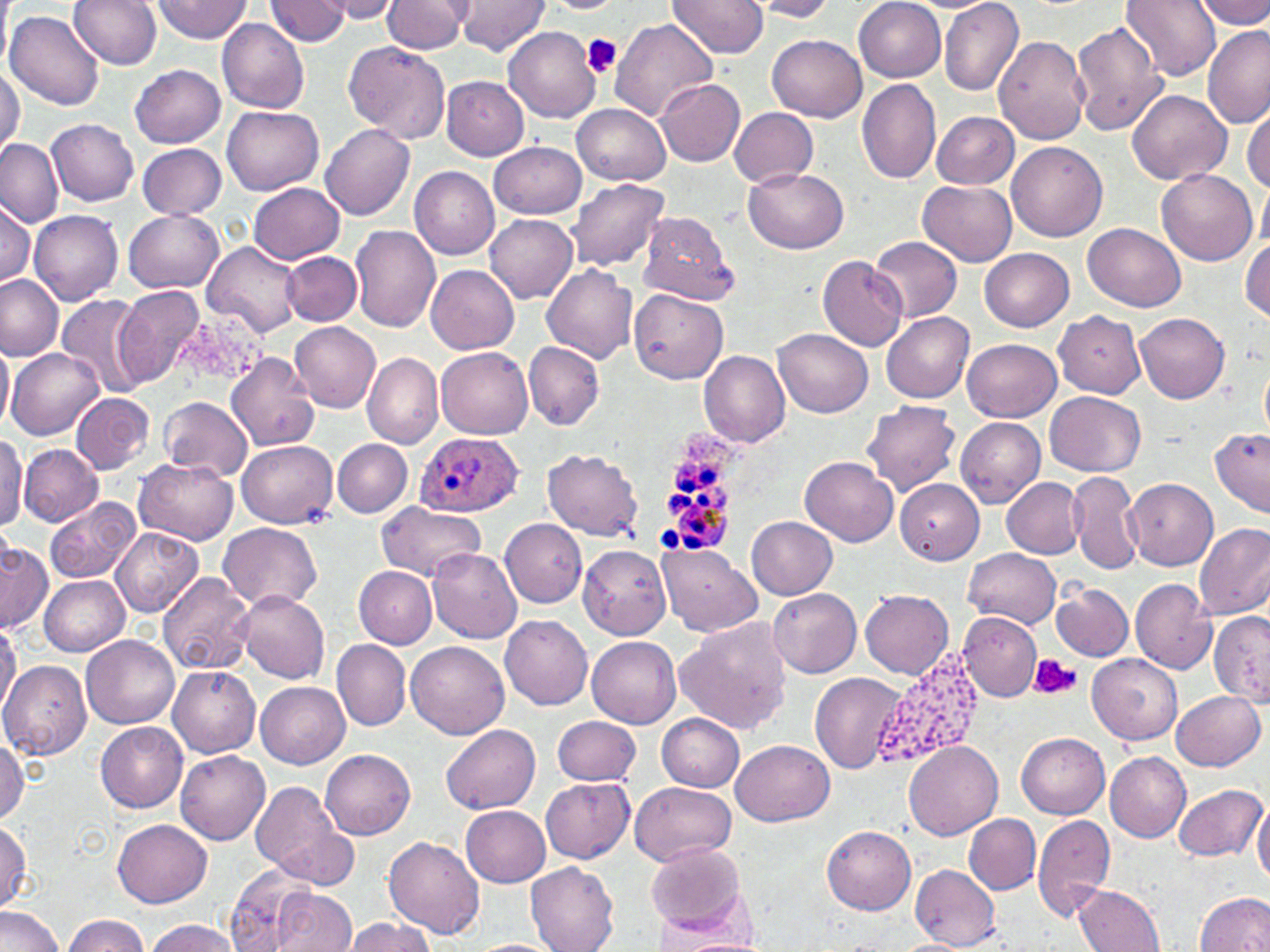

Approximate bounding boxes as named x1/y1/x2/y2 corners in pixels. Platelet locations: (x1=582, y1=34, x2=623, y2=79), (x1=1030, y1=655, x2=1083, y2=700). Uninfected red blood cell locations: (x1=0, y1=0, x2=10, y2=75), (x1=71, y1=0, x2=163, y2=69), (x1=319, y1=0, x2=404, y2=21), (x1=383, y1=0, x2=471, y2=53), (x1=455, y1=0, x2=550, y2=57), (x1=669, y1=0, x2=769, y2=57), (x1=1124, y1=0, x2=1221, y2=81), (x1=1196, y1=0, x2=1270, y2=30), (x1=151, y1=1, x2=252, y2=44), (x1=264, y1=1, x2=352, y2=44), (x1=539, y1=1, x2=625, y2=14), (x1=748, y1=1, x2=838, y2=21), (x1=854, y1=1, x2=945, y2=81), (x1=940, y1=1, x2=1024, y2=96), (x1=5, y1=9, x2=104, y2=109), (x1=607, y1=17, x2=718, y2=123), (x1=216, y1=18, x2=309, y2=115), (x1=1071, y1=19, x2=1169, y2=136), (x1=1201, y1=25, x2=1269, y2=126), (x1=503, y1=26, x2=600, y2=122), (x1=767, y1=32, x2=868, y2=120), (x1=993, y1=35, x2=1091, y2=145), (x1=342, y1=41, x2=450, y2=144), (x1=131, y1=64, x2=226, y2=147), (x1=0, y1=65, x2=25, y2=158), (x1=441, y1=76, x2=529, y2=160), (x1=655, y1=79, x2=745, y2=166), (x1=857, y1=79, x2=942, y2=185), (x1=1126, y1=89, x2=1230, y2=187), (x1=572, y1=104, x2=670, y2=185), (x1=1244, y1=104, x2=1270, y2=193), (x1=224, y1=106, x2=324, y2=197), (x1=730, y1=106, x2=818, y2=188), (x1=932, y1=112, x2=1019, y2=190), (x1=49, y1=119, x2=138, y2=207), (x1=321, y1=123, x2=415, y2=220), (x1=0, y1=137, x2=64, y2=227), (x1=488, y1=141, x2=586, y2=218), (x1=1007, y1=142, x2=1106, y2=243), (x1=137, y1=143, x2=227, y2=219), (x1=410, y1=167, x2=500, y2=259), (x1=744, y1=167, x2=848, y2=255), (x1=1155, y1=169, x2=1256, y2=266), (x1=1259, y1=176, x2=1270, y2=254), (x1=567, y1=178, x2=671, y2=272), (x1=918, y1=180, x2=1018, y2=267), (x1=247, y1=182, x2=345, y2=264), (x1=1, y1=197, x2=34, y2=288), (x1=28, y1=209, x2=122, y2=306), (x1=124, y1=211, x2=223, y2=293), (x1=639, y1=211, x2=739, y2=306), (x1=484, y1=215, x2=577, y2=304), (x1=1083, y1=222, x2=1187, y2=310), (x1=349, y1=225, x2=440, y2=332), (x1=870, y1=236, x2=964, y2=323), (x1=1242, y1=238, x2=1270, y2=322), (x1=203, y1=241, x2=303, y2=336), (x1=980, y1=248, x2=1073, y2=331), (x1=284, y1=252, x2=361, y2=325), (x1=817, y1=256, x2=908, y2=351), (x1=426, y1=264, x2=520, y2=354), (x1=542, y1=264, x2=639, y2=363), (x1=0, y1=274, x2=65, y2=361), (x1=115, y1=283, x2=205, y2=388), (x1=629, y1=288, x2=728, y2=385), (x1=55, y1=293, x2=151, y2=399), (x1=1054, y1=310, x2=1145, y2=400), (x1=882, y1=312, x2=975, y2=403), (x1=1135, y1=312, x2=1231, y2=403), (x1=291, y1=323, x2=381, y2=412), (x1=772, y1=328, x2=872, y2=417), (x1=0, y1=337, x2=12, y2=435), (x1=962, y1=338, x2=1062, y2=420), (x1=524, y1=342, x2=605, y2=431), (x1=6, y1=345, x2=103, y2=440), (x1=436, y1=347, x2=533, y2=438), (x1=699, y1=350, x2=791, y2=448), (x1=224, y1=351, x2=322, y2=453), (x1=363, y1=352, x2=443, y2=449), (x1=1260, y1=361, x2=1270, y2=441), (x1=1046, y1=390, x2=1146, y2=476), (x1=71, y1=393, x2=154, y2=475), (x1=159, y1=396, x2=252, y2=482), (x1=863, y1=400, x2=961, y2=494), (x1=955, y1=417, x2=1044, y2=507), (x1=1211, y1=427, x2=1270, y2=516), (x1=0, y1=432, x2=26, y2=531), (x1=236, y1=440, x2=337, y2=528), (x1=333, y1=440, x2=412, y2=516), (x1=17, y1=442, x2=104, y2=526), (x1=544, y1=449, x2=644, y2=543), (x1=800, y1=456, x2=898, y2=547), (x1=134, y1=458, x2=237, y2=545), (x1=1068, y1=471, x2=1143, y2=575), (x1=1003, y1=477, x2=1086, y2=559), (x1=1125, y1=478, x2=1217, y2=570), (x1=897, y1=480, x2=984, y2=564), (x1=44, y1=498, x2=142, y2=583), (x1=375, y1=502, x2=487, y2=580), (x1=747, y1=516, x2=837, y2=600), (x1=500, y1=519, x2=587, y2=608), (x1=1194, y1=521, x2=1270, y2=620), (x1=218, y1=523, x2=322, y2=610), (x1=110, y1=526, x2=203, y2=617), (x1=1, y1=540, x2=51, y2=633), (x1=656, y1=544, x2=762, y2=637), (x1=578, y1=545, x2=672, y2=640), (x1=426, y1=548, x2=522, y2=643), (x1=964, y1=548, x2=1061, y2=629), (x1=353, y1=566, x2=437, y2=648), (x1=157, y1=572, x2=256, y2=677), (x1=39, y1=573, x2=129, y2=656), (x1=1129, y1=579, x2=1218, y2=674), (x1=1051, y1=582, x2=1133, y2=661), (x1=767, y1=586, x2=861, y2=678), (x1=235, y1=590, x2=330, y2=683), (x1=860, y1=590, x2=955, y2=678), (x1=958, y1=611, x2=1041, y2=701), (x1=1210, y1=612, x2=1270, y2=704), (x1=500, y1=614, x2=593, y2=710), (x1=676, y1=617, x2=792, y2=734), (x1=0, y1=620, x2=19, y2=719), (x1=82, y1=634, x2=180, y2=728), (x1=588, y1=637, x2=681, y2=728), (x1=332, y1=640, x2=411, y2=731), (x1=406, y1=641, x2=508, y2=740), (x1=1087, y1=654, x2=1182, y2=744), (x1=0, y1=659, x2=91, y2=759), (x1=166, y1=663, x2=260, y2=757), (x1=812, y1=672, x2=907, y2=775), (x1=256, y1=682, x2=350, y2=768), (x1=1170, y1=690, x2=1265, y2=770), (x1=658, y1=714, x2=745, y2=791), (x1=553, y1=715, x2=641, y2=787), (x1=94, y1=719, x2=188, y2=812), (x1=440, y1=723, x2=539, y2=814), (x1=1017, y1=733, x2=1109, y2=817), (x1=0, y1=736, x2=27, y2=823), (x1=732, y1=739, x2=835, y2=826), (x1=902, y1=742, x2=1002, y2=839), (x1=321, y1=750, x2=416, y2=839), (x1=175, y1=751, x2=270, y2=845), (x1=1104, y1=751, x2=1190, y2=843), (x1=541, y1=777, x2=634, y2=864), (x1=249, y1=780, x2=353, y2=890), (x1=631, y1=782, x2=736, y2=867), (x1=1173, y1=785, x2=1265, y2=862), (x1=1253, y1=796, x2=1270, y2=891), (x1=459, y1=804, x2=551, y2=886), (x1=1032, y1=813, x2=1115, y2=923), (x1=965, y1=814, x2=1040, y2=895), (x1=112, y1=819, x2=212, y2=908), (x1=0, y1=820, x2=31, y2=911), (x1=821, y1=825, x2=916, y2=913), (x1=383, y1=834, x2=485, y2=938), (x1=646, y1=841, x2=745, y2=932), (x1=525, y1=862, x2=620, y2=952), (x1=911, y1=865, x2=1000, y2=949), (x1=224, y1=868, x2=335, y2=951), (x1=1073, y1=883, x2=1165, y2=952), (x1=271, y1=890, x2=357, y2=952), (x1=1196, y1=891, x2=1270, y2=951), (x1=0, y1=905, x2=66, y2=952), (x1=62, y1=915, x2=150, y2=952), (x1=342, y1=916, x2=435, y2=952), (x1=143, y1=918, x2=240, y2=952), (x1=652, y1=930, x2=772, y2=951), (x1=891, y1=938, x2=970, y2=952), (x1=466, y1=939, x2=565, y2=952). Plasmodium ovale-infected red blood cell locations: (x1=657, y1=425, x2=735, y2=551), (x1=414, y1=431, x2=523, y2=517). Slide-level diagnosis: Plasmodium ovale. Thin blood film. Captured at 1000x magnification. May-Grünwald-Giemsa-stained preparation. Image is 1270×952 pixels. Single field of view. Light microscopy.